Give the preparation type.
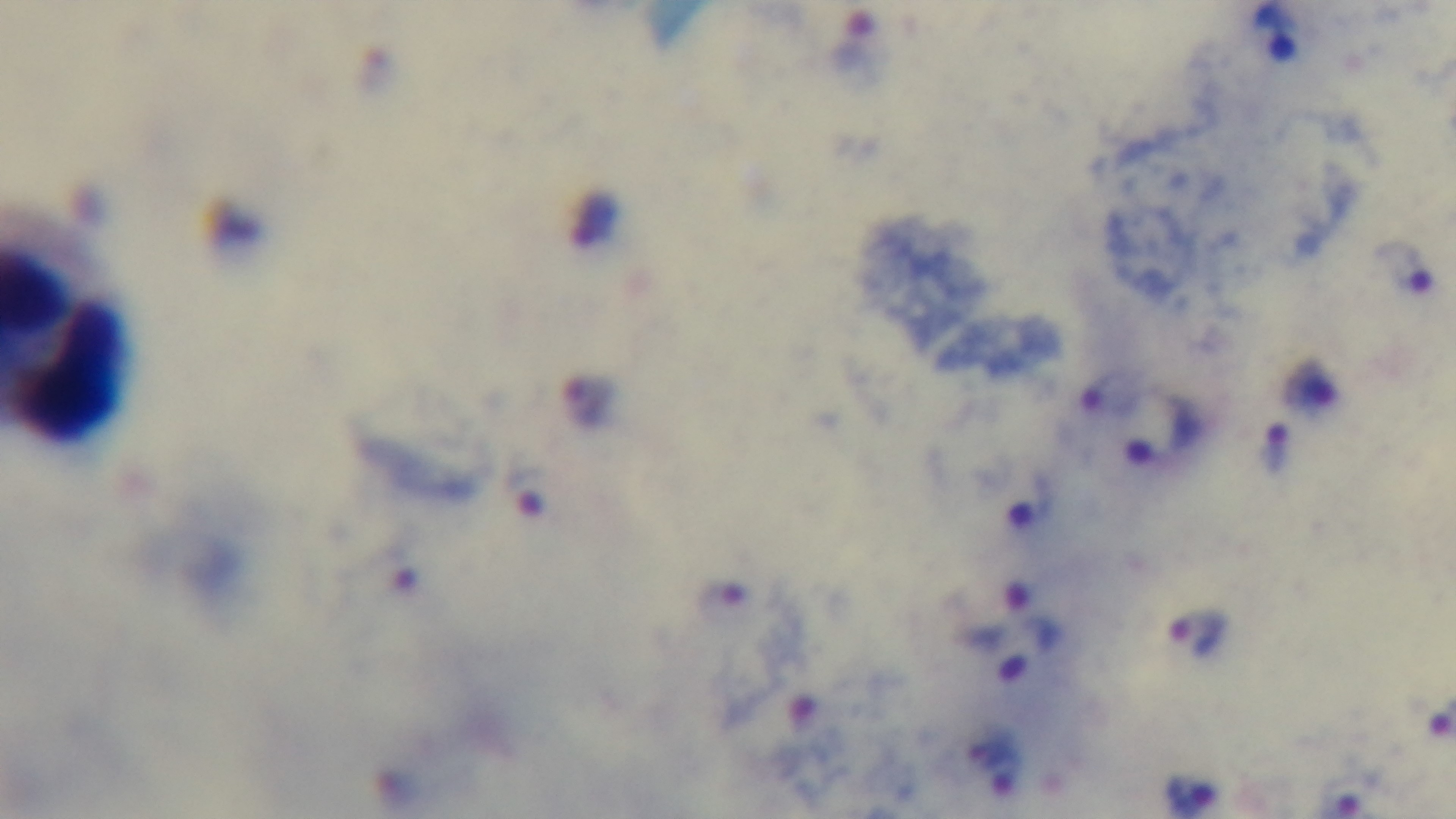

A thick smear.

Summary:
  - Modality: light microscopy
  - Malaria status: positive
  - Capture: mounted 4K digital camera
  - Stain: Giemsa
  - Objective: 100x oil immersion
  - Field of view: one from the slide